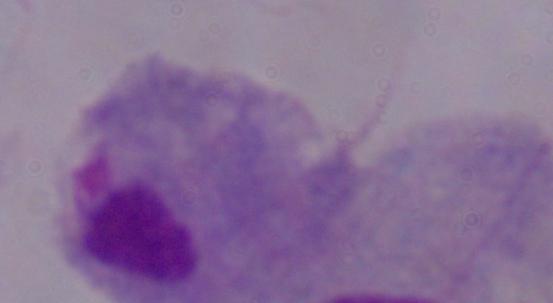
Photomicrograph. A trichomonad is shown. Captured at 1000x magnification.